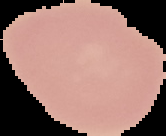

Summary:
  - Malaria status: uninfected
  - Image type: segmented cell region on a black background
  - Image size: 166×136 pixels
  - Preparation: thin blood smear